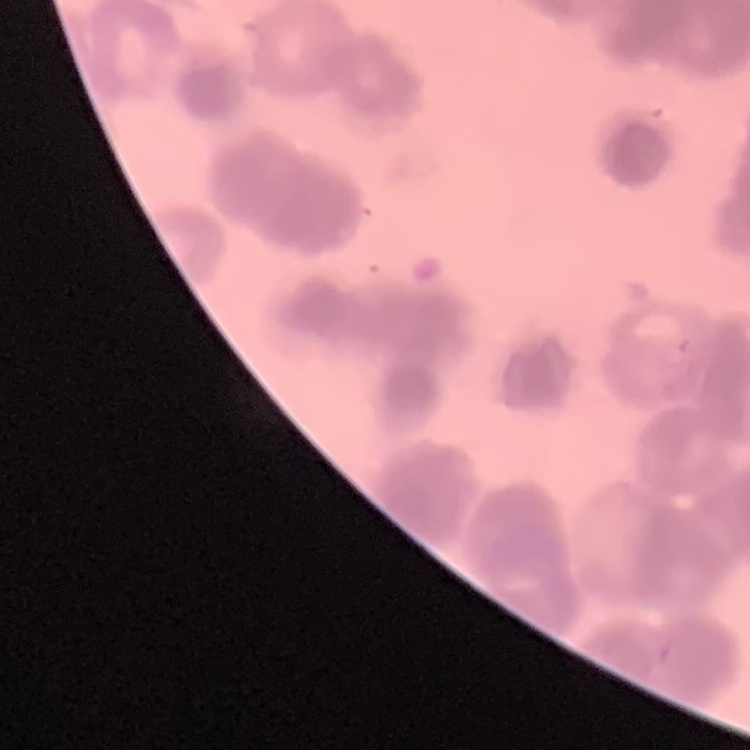
Summary:
  - Erythrocyte morphology: rouleaux formation
  - Stain: Field's or Giemsa
  - Image type: one tile cut from a larger photomicrograph
  - Preparation: thin blood film